Report the malaria status of this cell.
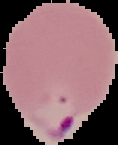
It is parasitized.

Summary:
  - Image size: 118×145 pixels
  - Preparation: thin blood smear
  - Image type: cell region segmented out of the field of view; surrounding area masked to black